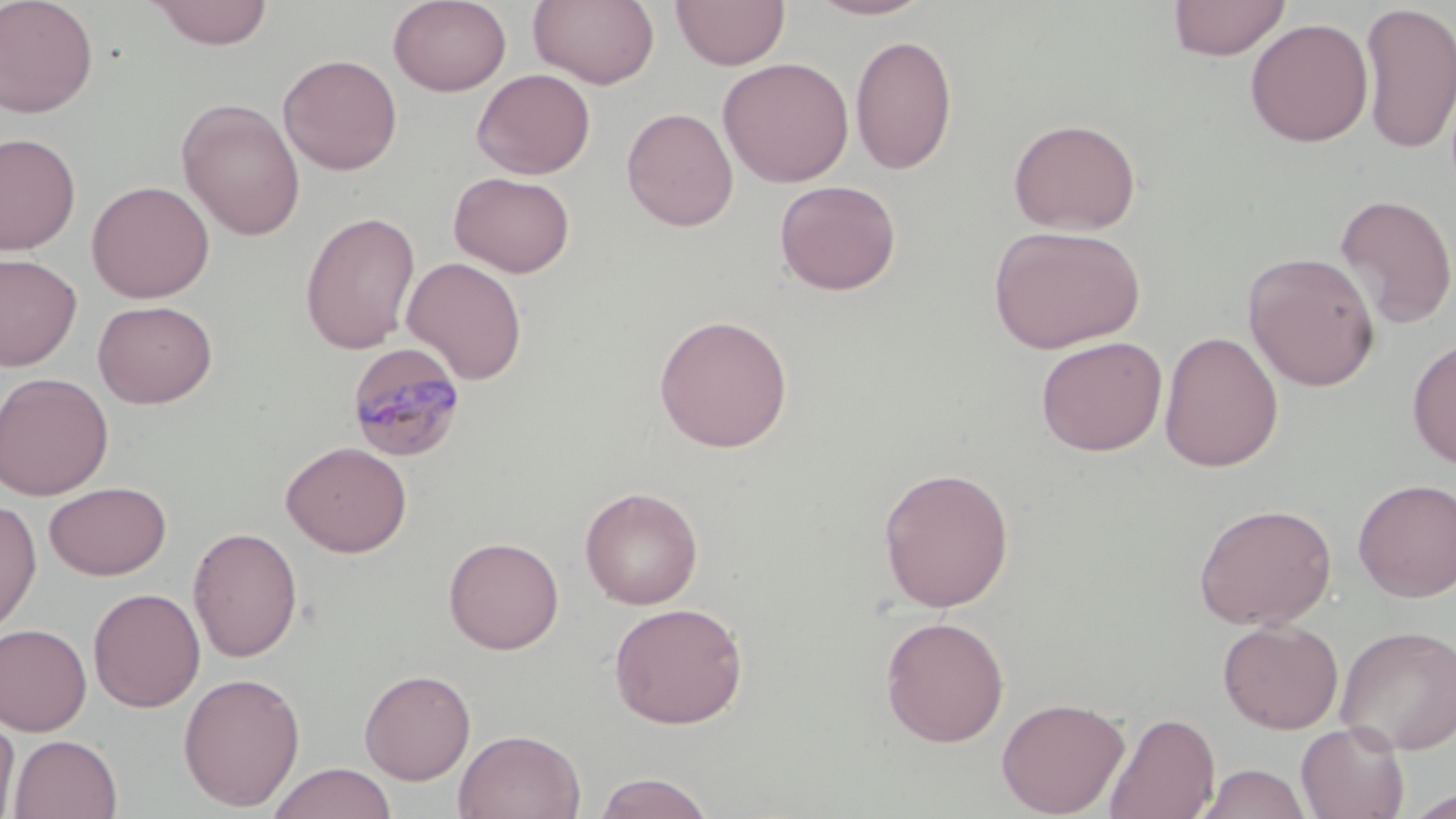

Summary:
  - Coordinate format: approximate bounding boxes as (x1, y1, x2, y2) in pixels
  - Plasmodium malariae-infected red blood cell locations: (346, 342, 468, 463)
  - Uninfected red blood cell locations: (0, 0, 99, 119), (147, 0, 274, 49), (388, 0, 512, 96), (528, 0, 660, 90), (670, 0, 791, 70), (806, 0, 936, 21), (1167, 0, 1291, 61), (1358, 2, 1456, 155), (1244, 17, 1375, 147), (850, 34, 957, 175), (277, 53, 402, 176), (717, 57, 855, 187), (472, 69, 596, 179), (176, 97, 306, 240), (621, 107, 739, 232), (1007, 117, 1142, 235), (0, 132, 81, 255), (449, 171, 576, 278), (774, 179, 901, 296), (86, 180, 215, 303), (1334, 194, 1456, 328), (300, 211, 421, 355), (988, 224, 1146, 354), (1243, 251, 1381, 392), (0, 252, 82, 371), (401, 256, 528, 384), (92, 299, 217, 408), (653, 314, 794, 453), (1159, 330, 1284, 473), (1035, 335, 1168, 456), (1407, 337, 1456, 469), (0, 371, 113, 500), (280, 441, 413, 558), (877, 466, 1015, 613), (1353, 478, 1456, 602), (44, 481, 171, 580), (579, 486, 704, 610), (0, 498, 42, 637), (1193, 502, 1337, 630), (188, 526, 303, 662), (443, 536, 565, 654), (87, 587, 205, 712), (608, 601, 749, 729), (880, 616, 1009, 747), (1217, 619, 1344, 734), (0, 623, 92, 736), (1335, 623, 1456, 754), (359, 668, 476, 785), (177, 671, 305, 811), (996, 696, 1130, 817), (1103, 711, 1220, 819), (0, 716, 20, 818), (1296, 722, 1409, 819), (454, 728, 586, 818), (8, 734, 123, 819), (266, 762, 398, 819), (1197, 764, 1313, 819), (592, 771, 716, 818), (1403, 787, 1456, 818)
  - Slide-level diagnosis: Plasmodium malariae
  - Magnification: 1000x
  - Preparation: thin blood smear
  - Image size: 1456×819 pixels
  - Stain: May-Grünwald-Giemsa
  - Modality: optical microscopy
  - Field of view: single